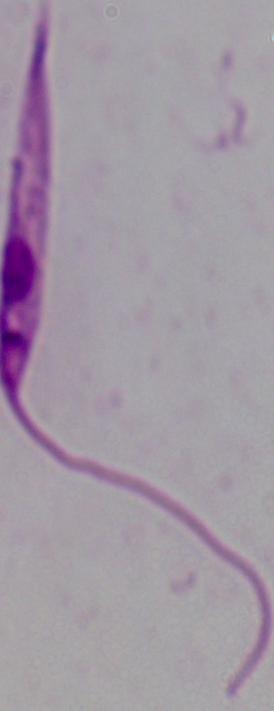

identification = Leishmania
modality = micrograph
magnification = 1000x